Locate every leukocyte (white blood cell).
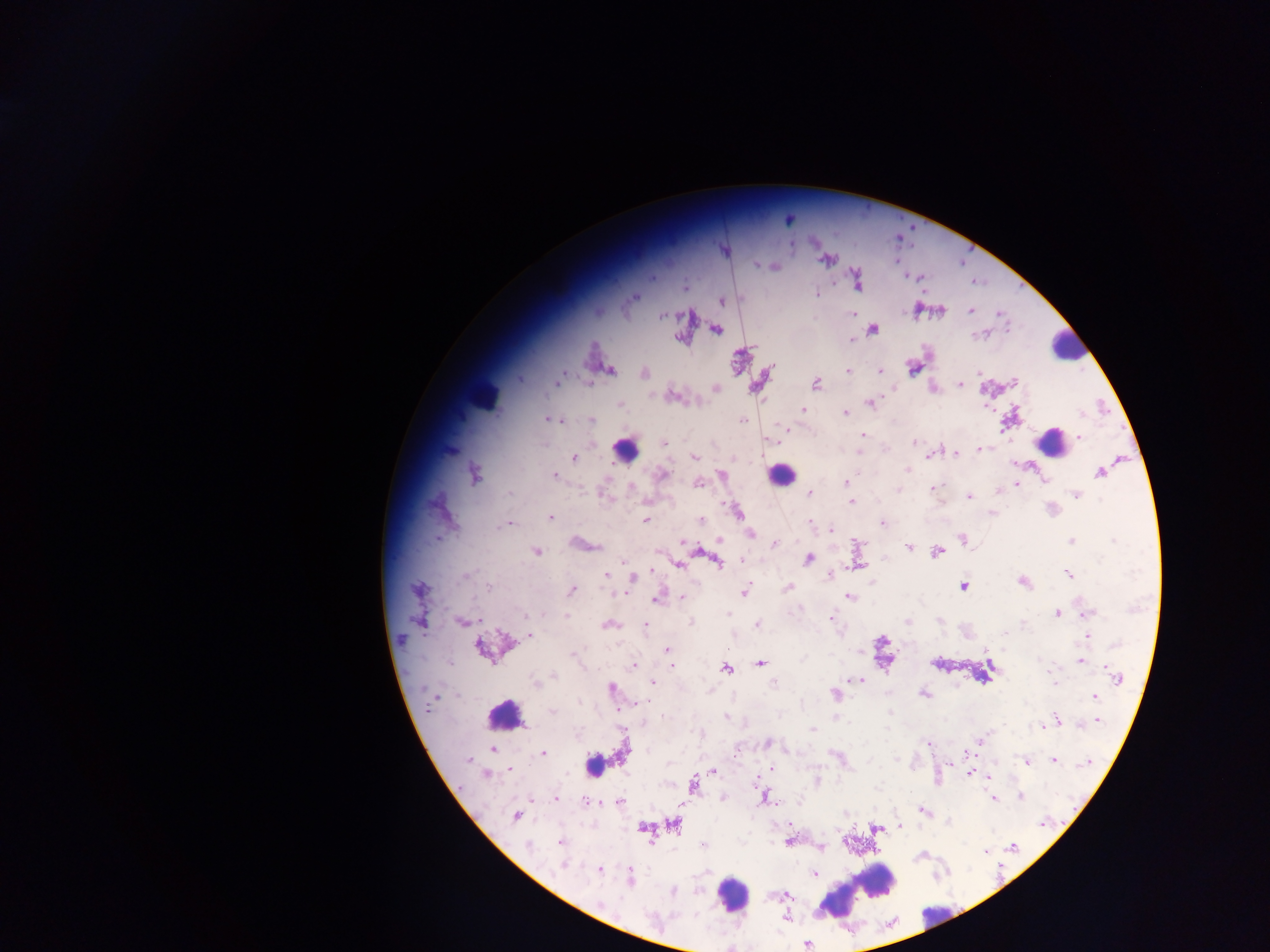
Approximate centers as x y in pixels.
Leukocytes: 1068 346; 483 393; 1050 437; 625 449; 781 474; 506 715; 595 765; 875 877; 732 895; 838 900; 936 911.

{
  "country": "Ghana",
  "preparation": "thick blood smear",
  "capture": "mobile-phone photograph through a microscope",
  "image_size": "1270×952 pixels",
  "malaria_parasite_locations": "approximate centers as x y in pixels: 788 219; 791 245; 826 260; 756 265; 774 267; 857 281; 685 286; 816 293; 633 297; 722 301; 970 310; 941 311; 853 314; 663 315; 716 330; 873 330; 852 339; 913 368; 610 370; 848 371; 880 371; 644 373; 978 373; 520 379; 560 380; 1013 382; 960 383; 816 384; 715 388; 673 397; 871 403; 619 405; 802 409; 845 413; 1080 414; 552 420; 591 420; 742 420; 862 435; 1079 437; 664 443; 915 443; 980 449; 860 452; 956 453; 930 456; 694 457; 574 458; 907 469; 1099 473; 475 474; 662 474; 554 475; 722 475; 846 483; 698 484; 1016 485; 631 487; 934 488; 899 489; 998 490; 509 493; 809 493; 1077 494; 969 496; 851 502; 736 511; 991 513; 550 517; 700 520; 646 521; 810 523; 509 524; 883 524; 831 530; 750 533; 962 539; 720 540; 1071 541; 1114 541; 774 543; 908 548; 537 552; 937 552; 809 559; 718 561; 679 565; 857 565; 1068 574; 606 575; 465 576; 828 576; 633 578; 1023 582; 871 583; 490 587; 787 587; 964 587; 418 589; 571 591; 744 593; 683 596; 849 596; 657 600; 728 614; 1058 614; 1088 614; 566 616; 831 618; 462 621; 939 621; 907 622; 691 623; 1023 624; 609 625; 757 625; 645 627; 1004 634; 531 636; 1088 636; 883 641; 480 648; 667 650; 861 651; 1081 661; 760 663; 935 664; 634 665; 671 665; 989 667; 1052 667; 727 669; 554 676; 1118 677; 859 681; 535 683; 653 683; 773 683; 1054 683; 611 689; 835 694; 923 694; 1095 696; 579 703; 553 712; 726 716; 1056 718; 1098 721; 1042 726; 813 730; 980 739; 767 743; 928 743; 494 749; 624 752; 543 753; 836 756; 469 760; 1053 760; 1026 762; 1087 764; 510 769; 772 769; 714 771; 487 775; 970 775; 990 777; 817 781; 694 784; 764 796; 1020 797; 556 798; 998 798; 994 799; 586 801; 620 802; 922 810; 515 817; 1042 824; 675 825; 643 826; 901 827; 876 828; 789 841; 560 842; 528 845; 704 845; 821 847; 1013 847; 985 850; 564 865; 599 869; 815 873; 631 876; 672 891; 600 904; 786 919; 806 944",
  "field_of_view": "single"
}